Locate platelets.
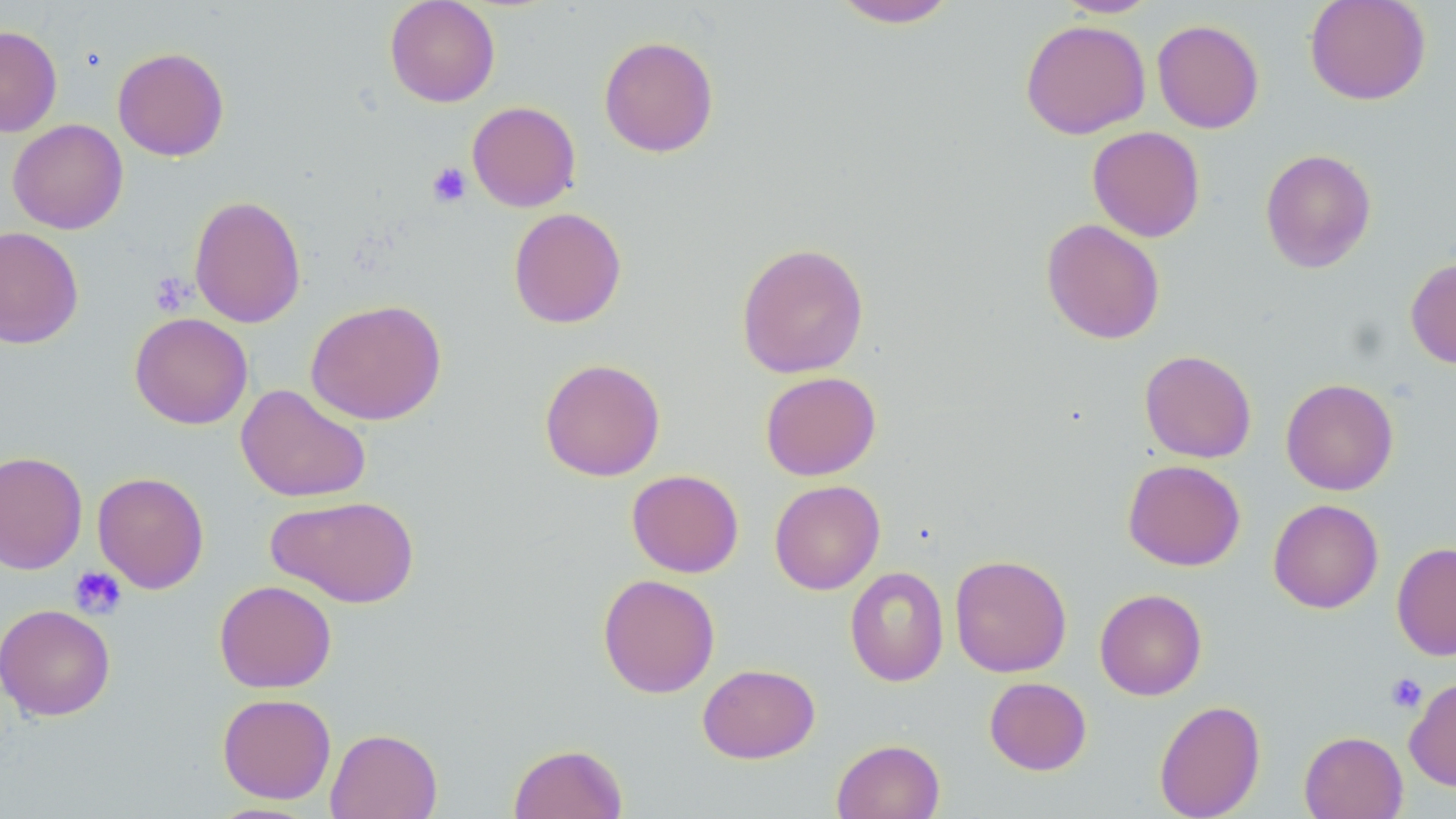
Approximate bounding boxes as (x1, y1, x2, y2) in pixels.
Platelets: (427, 162, 471, 207), (150, 271, 194, 317), (69, 565, 127, 619), (1385, 673, 1427, 713).

slide-level diagnosis = no evidence of blood parasites
preparation = thin blood smear
uninfected red blood cell locations = approximate bounding boxes as (x1, y1, x2, y2) in pixels: (384, 0, 500, 107), (829, 0, 962, 28), (1053, 0, 1159, 18), (1304, 0, 1431, 105), (1020, 19, 1151, 140), (1151, 19, 1265, 133), (0, 26, 62, 137), (598, 35, 720, 158), (113, 47, 229, 161), (466, 101, 581, 212), (7, 119, 128, 234), (1087, 126, 1205, 242), (1260, 148, 1377, 273), (188, 194, 306, 329), (508, 207, 627, 328), (1041, 218, 1165, 344), (0, 226, 84, 349), (736, 242, 870, 379), (1406, 257, 1456, 369), (305, 299, 448, 426), (129, 312, 253, 429), (1139, 350, 1256, 463), (539, 357, 666, 482), (760, 371, 881, 480), (1281, 378, 1399, 496), (236, 384, 372, 503), (0, 450, 88, 575), (1123, 459, 1246, 571), (627, 469, 744, 578), (93, 471, 209, 594), (769, 480, 885, 595), (267, 494, 419, 608), (1268, 499, 1383, 614), (1391, 541, 1456, 661), (950, 554, 1072, 677), (844, 566, 949, 686), (597, 574, 721, 698), (214, 579, 337, 693), (1094, 588, 1207, 700), (0, 603, 116, 721), (698, 663, 820, 763), (984, 677, 1092, 775), (1404, 677, 1456, 792), (217, 693, 337, 803), (1153, 699, 1266, 819), (325, 727, 443, 819), (1299, 730, 1408, 819), (832, 738, 945, 819), (508, 743, 628, 819), (205, 801, 323, 818)
field of view = single
modality = optical microscopy
magnification = 1000x
stain = May-Grünwald-Giemsa
image size = 1456×819 pixels